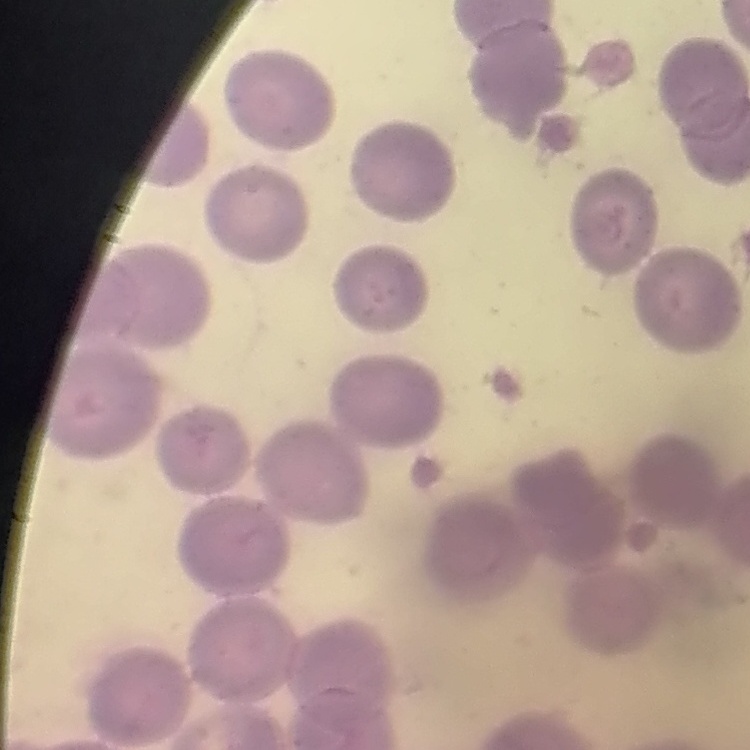

red blood cell morphology = no rouleaux formation
stain = Field's or Giemsa
image type = one tile cut from a larger photomicrograph
preparation = thin blood smear